Describe the morphology of the red blood cells.
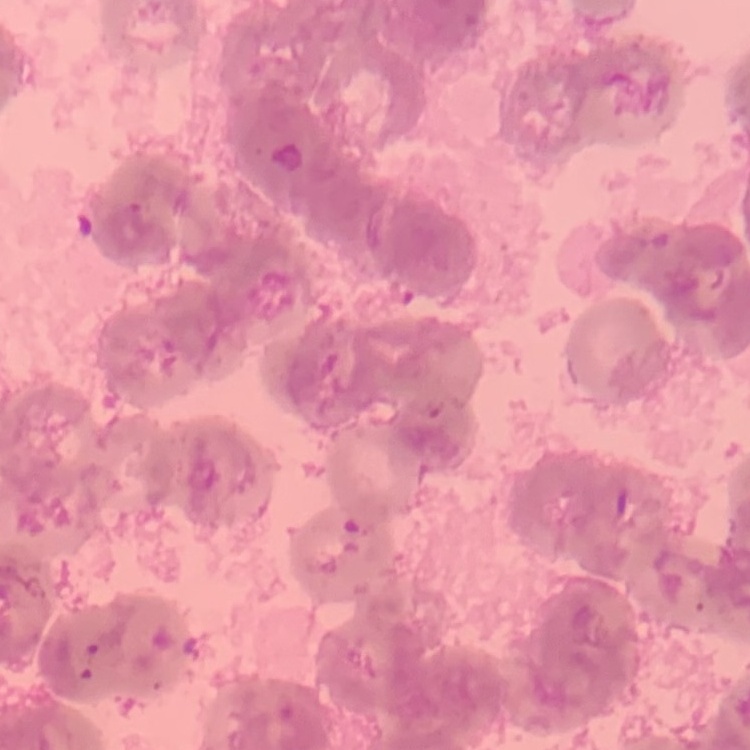
Rouleaux formation.

{
  "stain": "Field's or Giemsa",
  "preparation": "thin peripheral smear",
  "image_type": "square crop of a larger photomicrograph"
}